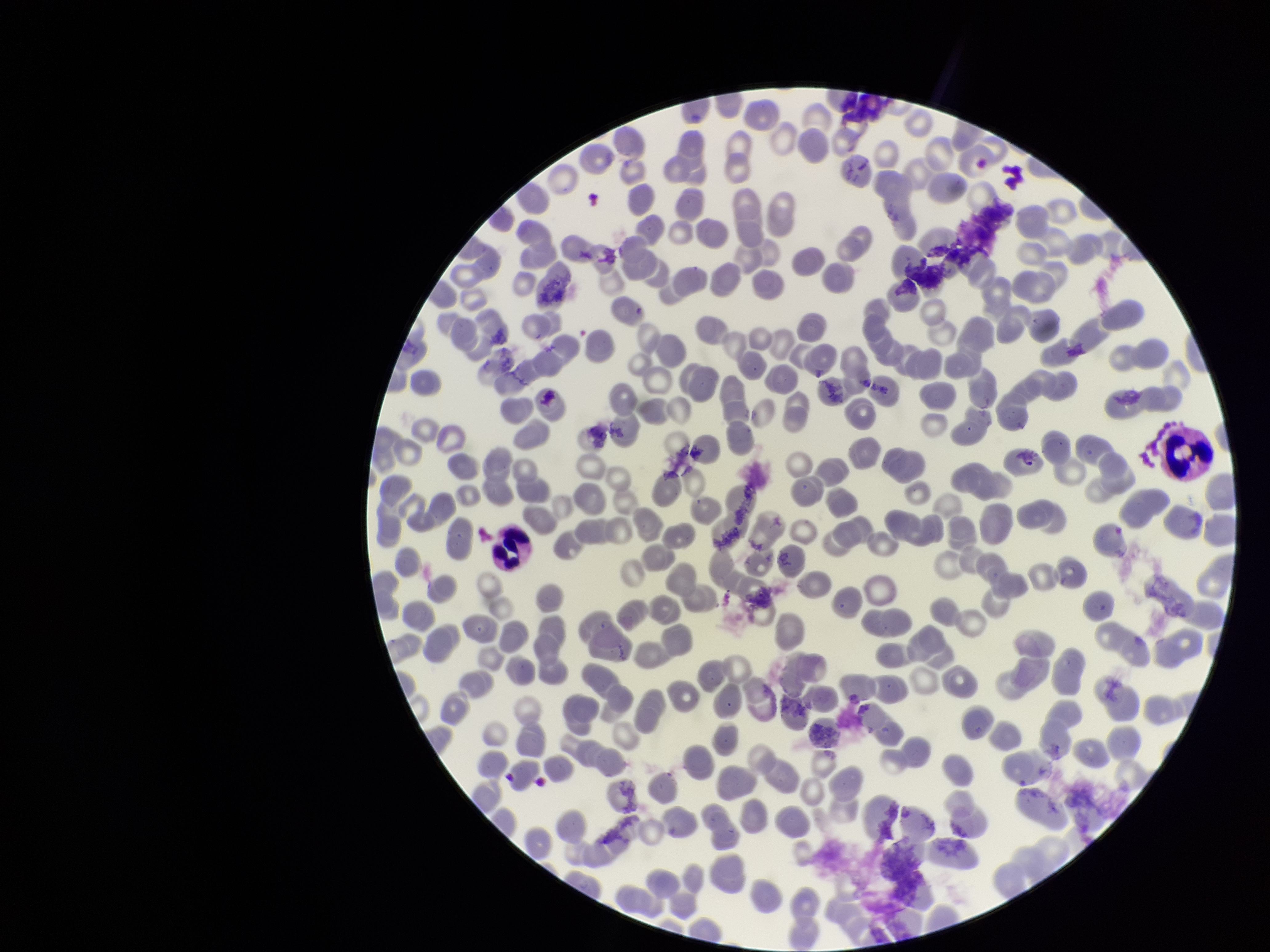

stain = Giemsa
capture = smartphone photograph through the microscope eyepiece
field of view = single
preparation = thin smear
image size = 1270×952 pixels
red blood cell count = 278
parasitized red blood cell count = 0
parasitized red blood cells = none seen
patient malaria status = negative